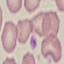

Summary:
  - Result: no malaria parasites seen
  - Capture: smartphone camera at the microscope eyepiece
  - Image type: automatically extracted cell patch, resized to 64 × 64 pixels
  - Stain: Giemsa
  - Preparation: thin blood smear